Give the position of every Plasmodium parasite.
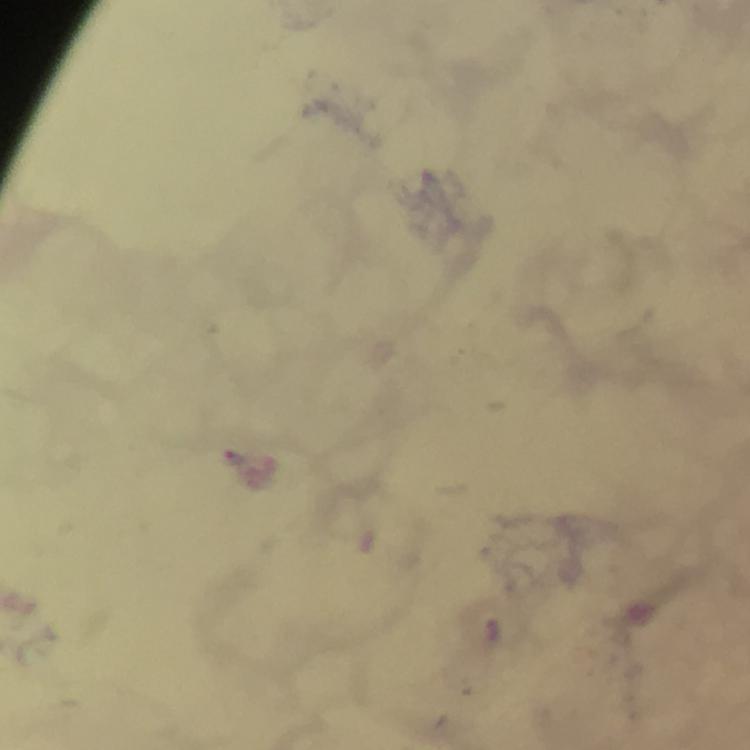

Approximate centers as [x, y] in pixels.
Plasmodium parasites: [231, 458].

capture: smartphone mounted on the microscope
stain: Giemsa
context: from a malaria diagnostic workup
image_size: 750×750 pixels
magnification: 100x
preparation: thick blood smear
immersion_oil: used
cropped_from: a single field of view